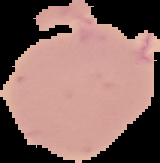

From a thin blood smear. The area outside the segmented cell region is set to black. Malaria status: uninfected. Image is 160×163 pixels.